Locate every Plasmodium falciparum-infected red blood cell.
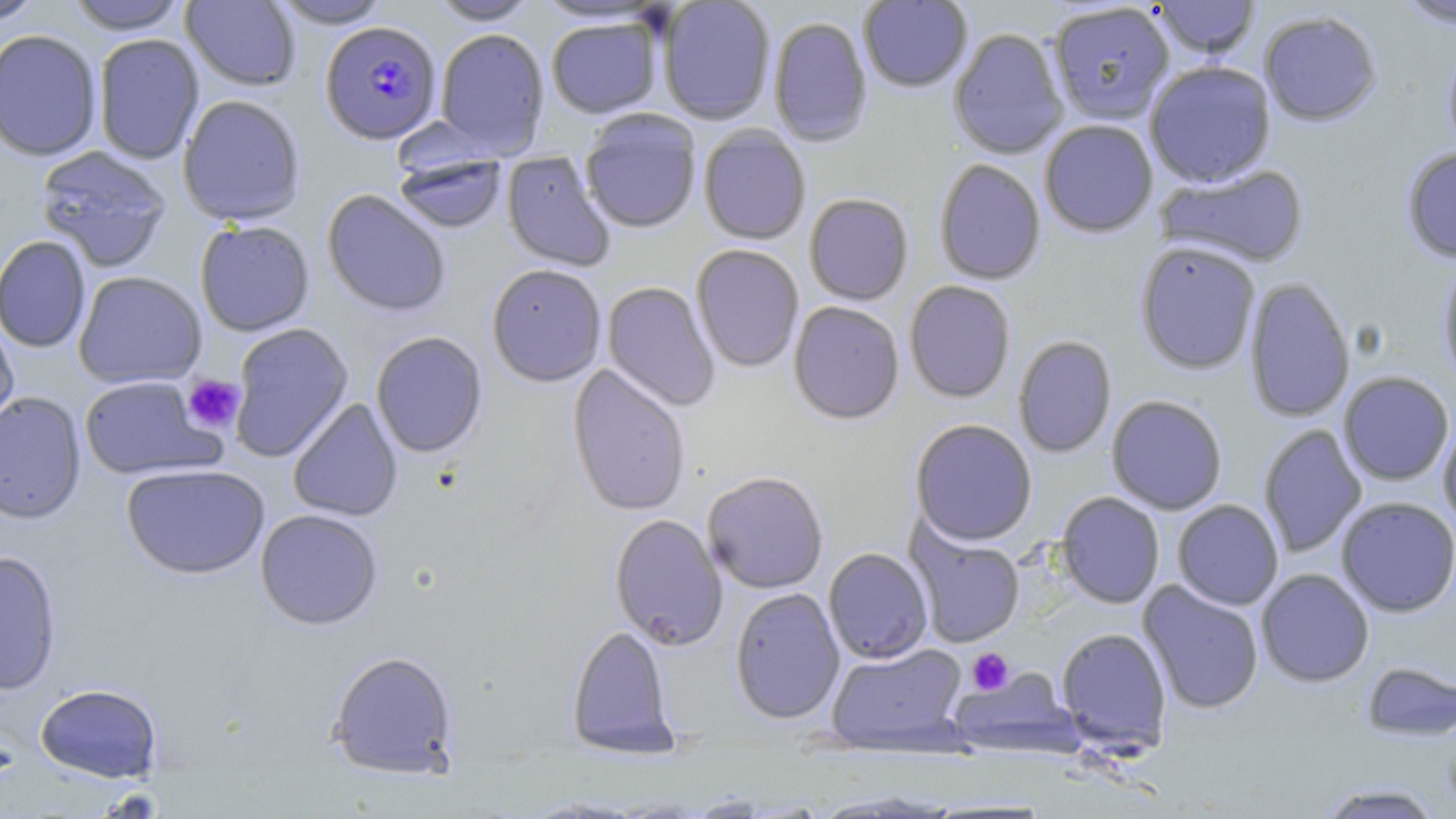

Approximate bounding boxes as named x1/y1/x2/y2 corners in pixels.
Plasmodium falciparum-infected red blood cells: (x1=320, y1=22, x2=442, y2=145).

slide-level diagnosis = Plasmodium falciparum
image size = 1456×819 pixels
preparation = thin blood smear
field of view = one of a larger specimen
modality = optical microscopy
uninfected red blood cell locations = approximate bounding boxes as named x1/y1/x2/y2 corners in pixels: (x1=0, y1=0, x2=44, y2=26), (x1=181, y1=0, x2=301, y2=91), (x1=268, y1=0, x2=393, y2=29), (x1=428, y1=0, x2=540, y2=25), (x1=858, y1=0, x2=973, y2=93), (x1=1394, y1=0, x2=1456, y2=30), (x1=64, y1=1, x2=188, y2=34), (x1=658, y1=1, x2=776, y2=126), (x1=1150, y1=1, x2=1261, y2=60), (x1=1048, y1=4, x2=1175, y2=126), (x1=1259, y1=11, x2=1382, y2=127), (x1=546, y1=17, x2=664, y2=119), (x1=768, y1=17, x2=873, y2=148), (x1=435, y1=28, x2=550, y2=159), (x1=948, y1=28, x2=1068, y2=160), (x1=0, y1=29, x2=102, y2=161), (x1=942, y1=29, x2=1053, y2=287), (x1=93, y1=33, x2=204, y2=165), (x1=1442, y1=45, x2=1456, y2=162), (x1=1144, y1=61, x2=1277, y2=188), (x1=177, y1=94, x2=306, y2=226), (x1=580, y1=111, x2=702, y2=234), (x1=1039, y1=120, x2=1158, y2=238), (x1=698, y1=126, x2=811, y2=245), (x1=34, y1=145, x2=173, y2=273), (x1=1401, y1=146, x2=1456, y2=263), (x1=393, y1=150, x2=508, y2=235), (x1=501, y1=152, x2=616, y2=272), (x1=934, y1=159, x2=1046, y2=285), (x1=1154, y1=163, x2=1310, y2=268), (x1=321, y1=189, x2=451, y2=317), (x1=803, y1=193, x2=913, y2=306), (x1=195, y1=220, x2=315, y2=337), (x1=0, y1=235, x2=91, y2=353), (x1=1134, y1=240, x2=1261, y2=375), (x1=691, y1=245, x2=804, y2=373), (x1=1437, y1=255, x2=1456, y2=389), (x1=486, y1=264, x2=607, y2=387), (x1=73, y1=271, x2=207, y2=389), (x1=1243, y1=277, x2=1355, y2=423), (x1=903, y1=280, x2=1016, y2=403), (x1=602, y1=281, x2=719, y2=412), (x1=788, y1=302, x2=905, y2=425), (x1=0, y1=315, x2=19, y2=439), (x1=228, y1=323, x2=354, y2=462), (x1=370, y1=331, x2=488, y2=458), (x1=1012, y1=335, x2=1117, y2=459), (x1=567, y1=364, x2=691, y2=517), (x1=1338, y1=371, x2=1455, y2=486), (x1=78, y1=375, x2=224, y2=481), (x1=0, y1=392, x2=86, y2=525), (x1=1106, y1=394, x2=1228, y2=515), (x1=287, y1=398, x2=403, y2=522), (x1=1437, y1=415, x2=1456, y2=534), (x1=910, y1=419, x2=1038, y2=546), (x1=1258, y1=424, x2=1367, y2=558), (x1=121, y1=463, x2=270, y2=580), (x1=702, y1=471, x2=828, y2=594), (x1=1056, y1=492, x2=1165, y2=609), (x1=1336, y1=497, x2=1456, y2=617), (x1=1172, y1=499, x2=1284, y2=610), (x1=255, y1=509, x2=383, y2=630), (x1=609, y1=513, x2=728, y2=651), (x1=906, y1=523, x2=1025, y2=648), (x1=823, y1=547, x2=933, y2=664), (x1=0, y1=550, x2=62, y2=695), (x1=1256, y1=568, x2=1374, y2=687), (x1=1138, y1=580, x2=1264, y2=715), (x1=730, y1=587, x2=845, y2=725), (x1=566, y1=625, x2=678, y2=759), (x1=1056, y1=626, x2=1172, y2=754), (x1=826, y1=642, x2=968, y2=755), (x1=326, y1=650, x2=459, y2=780), (x1=1361, y1=661, x2=1455, y2=742), (x1=948, y1=667, x2=1081, y2=758), (x1=35, y1=683, x2=163, y2=783), (x1=1313, y1=783, x2=1446, y2=818)
stain = May-Grünwald-Giemsa
platelet locations = approximate bounding boxes as named x1/y1/x2/y2 corners in pixels: (x1=181, y1=374, x2=245, y2=433), (x1=967, y1=647, x2=1013, y2=694)
magnification = 1000x